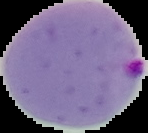

image size = 148×133 pixels
preparation = thin blood smear
malaria status = parasitized
image type = cell region segmented out of the field of view; surrounding area masked to black